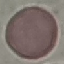

result = no malaria parasites detected
stain = Giemsa
capture = smartphone through the microscope eyepiece
preparation = thin smear
image type = automatically extracted cell patch, resized to 64 × 64 pixels